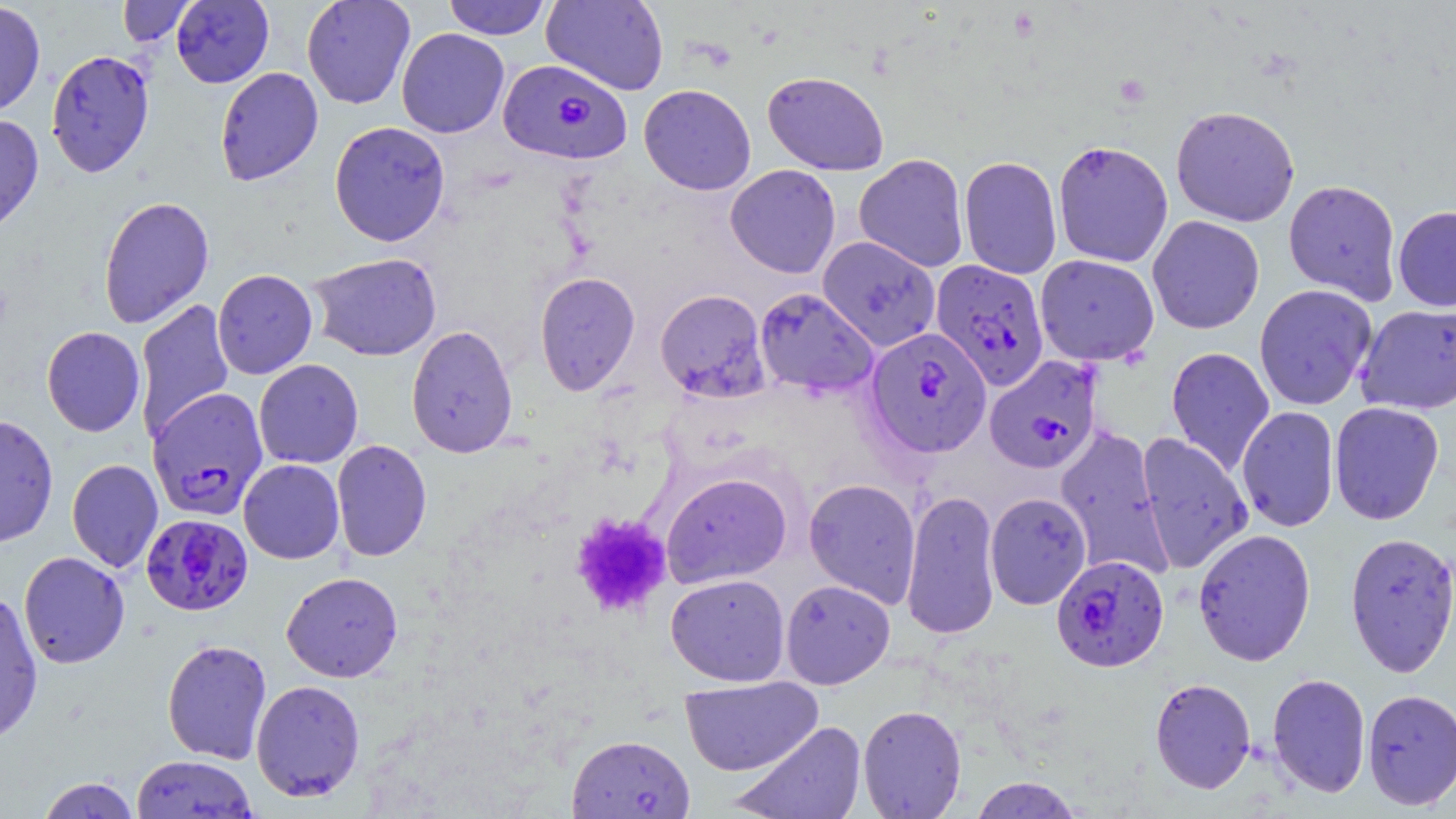

Summary:
  - Coordinate format: approximate bounding boxes as [x1, y1, x2, y2] in pixels
  - Plasmodium falciparum-infected red blood cell locations: [499, 59, 631, 166], [931, 259, 1049, 390], [865, 327, 992, 458], [983, 356, 1102, 474], [148, 387, 268, 520], [141, 514, 253, 616], [1051, 555, 1169, 672], [566, 733, 695, 818]
  - Uninfected red blood cell locations: [117, 0, 196, 47], [171, 0, 274, 88], [301, 0, 416, 109], [443, 0, 552, 40], [540, 0, 670, 96], [0, 1, 46, 116], [396, 28, 509, 138], [45, 49, 155, 178], [215, 67, 323, 186], [762, 71, 889, 175], [639, 83, 756, 195], [1170, 105, 1300, 227], [1160, 106, 1275, 335], [0, 114, 44, 236], [329, 121, 451, 247], [1052, 140, 1174, 268], [854, 154, 970, 272], [959, 156, 1062, 280], [725, 164, 841, 278], [1283, 179, 1402, 304], [98, 195, 215, 329], [1392, 206, 1456, 311], [1147, 215, 1265, 334], [817, 236, 940, 351], [309, 252, 442, 361], [1035, 254, 1159, 365], [212, 269, 318, 379], [534, 271, 640, 395], [1254, 284, 1378, 411], [754, 287, 878, 398], [655, 289, 770, 403], [134, 298, 234, 441], [1355, 303, 1456, 415], [406, 325, 519, 459], [42, 326, 146, 437], [1166, 346, 1275, 476], [253, 359, 364, 469], [1329, 401, 1445, 525], [1236, 405, 1339, 533], [1, 414, 58, 548], [1054, 425, 1173, 580], [1136, 432, 1253, 574], [331, 440, 432, 561], [67, 459, 163, 573], [238, 459, 344, 564], [661, 472, 792, 587], [804, 478, 921, 608], [901, 489, 1002, 640], [985, 492, 1091, 610], [1192, 528, 1316, 666], [1344, 531, 1456, 677], [18, 551, 130, 669], [281, 571, 403, 682], [665, 573, 790, 686], [780, 579, 895, 689], [0, 590, 43, 744], [162, 639, 273, 764], [1267, 672, 1371, 797], [679, 676, 822, 776], [1150, 677, 1256, 793], [250, 679, 366, 801], [1362, 688, 1456, 810], [857, 704, 967, 818], [732, 720, 866, 819], [131, 755, 257, 817], [37, 775, 141, 819], [968, 776, 1086, 818]
  - Platelet locations: [1113, 72, 1151, 108], [569, 512, 673, 619]
  - Slide-level diagnosis: Plasmodium falciparum
  - Image size: 1456×819 pixels
  - Stain: May-Grünwald-Giemsa
  - Field of view: one of a larger specimen
  - Preparation: thin blood film
  - Magnification: 1000x
  - Modality: optical microscopy